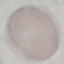
Summary:
  - Result: negative for malaria parasites
  - Image type: automatically extracted cell patch, resized to 64 × 64 pixels
  - Preparation: thin blood smear
  - Stain: Giemsa
  - Capture: smartphone camera at the microscope eyepiece